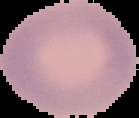
From a thin blood film. Result: no Plasmodium parasites seen. Segmented cell region on a black background. Image is 139×118 pixels.